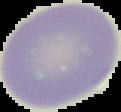
Summary:
  - Image size: 121×112 pixels
  - Image type: segmented cell region with the area outside set to black
  - Malaria status: uninfected
  - Preparation: thin blood film